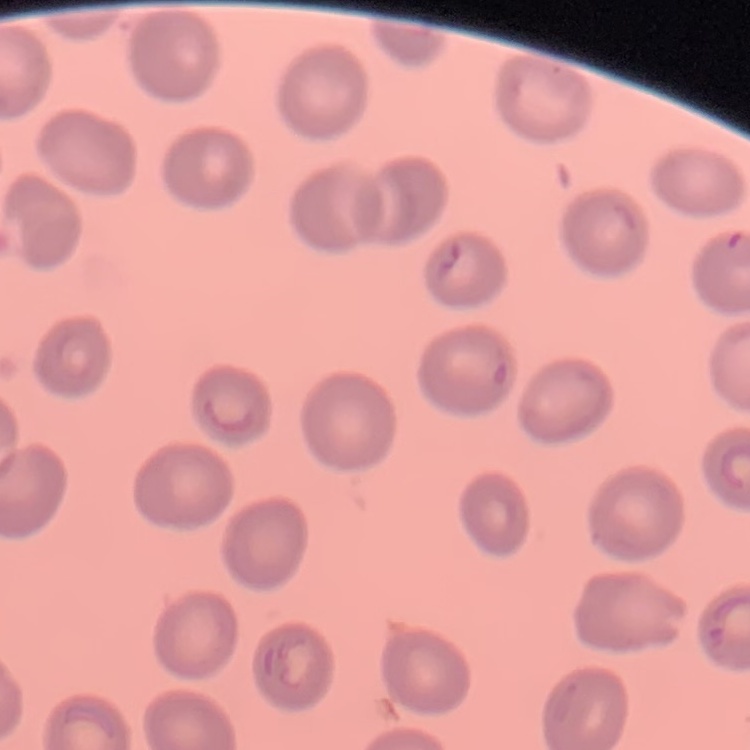

Summary:
  - Red blood cell morphology: no rouleaux formation
  - Image type: square crop of a larger photomicrograph
  - Stain: Field's or Giemsa
  - Preparation: thin blood film